State which parasite is depicted.
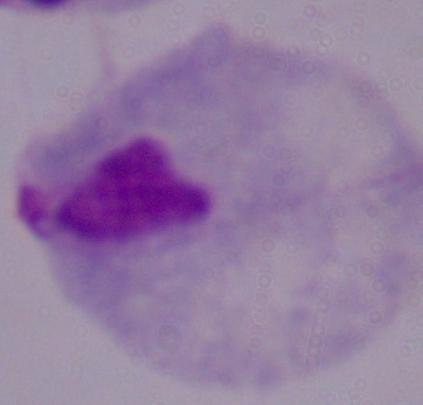

A trichomonad.

Summary:
  - Modality: micrograph
  - Magnification: 1000x